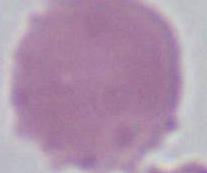
A red blood cell is seen. Micrograph. Captured at 1000x magnification.